Classify this cell by malaria status.
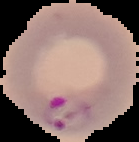
Parasitized.

{
  "image_size": "139×142 pixels",
  "preparation": "thin blood film",
  "image_type": "segmented cell region on a black background"
}